Locate and identify every blood parasite.
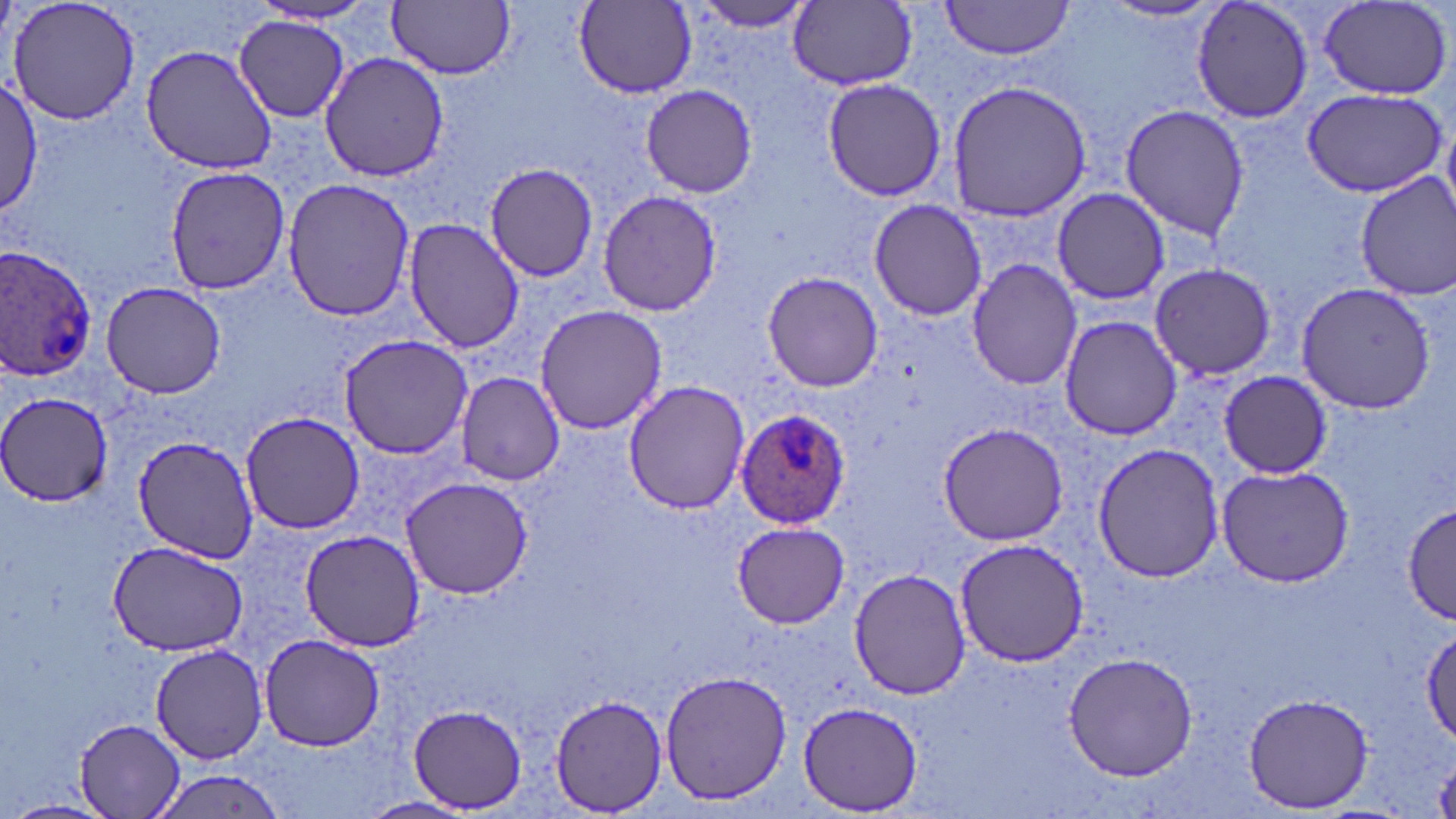
Approximate bounding boxes as (x1,y1)-(x2,y2) corner pairs in pixels.
Plasmodium ovale-infected red blood cells: (0,246)-(99,381), (736,411)-(850,527).
No Plasmodium falciparum, Plasmodium malariae, Plasmodium vivax, Babesia divergens, or Trypanosoma brucei observed.

slide_level_diagnosis: Plasmodium ovale
uninfected_red_blood_cell_locations: 'approximate bounding boxes as (x1,y1)-(x2,y2) corner pairs in pixels: (5,0)-(142,126), (686,0)-(817,34), (940,0)-(1074,60), (1190,0)-(1315,124), (388,1)-(516,79), (1101,1)-(1223,23), (575,2)-(697,97), (791,2)-(919,89), (1318,2)-(1453,100), (246,3)-(382,29), (235,17)-(350,123), (141,45)-(274,174), (320,52)-(448,182), (1,78)-(42,217), (820,79)-(948,202), (946,79)-(1095,221), (641,85)-(759,197), (1301,87)-(1448,199), (1119,103)-(1248,241), (485,163)-(600,280), (165,166)-(291,296), (1354,172)-(1456,301), (282,177)-(416,322), (1051,187)-(1170,306), (596,190)-(724,316), (867,199)-(988,320), (404,218)-(522,354), (967,260)-(1083,392), (1149,262)-(1278,381), (761,270)-(884,392), (101,280)-(227,399), (1296,282)-(1436,415), (534,304)-(667,434), (1058,315)-(1181,441), (340,334)-(474,459), (1217,370)-(1334,477), (456,373)-(564,486), (624,380)-(749,514), (2,394)-(114,508), (240,410)-(365,534), (938,422)-(1068,546), (134,437)-(260,564), (1091,442)-(1226,582), (1215,463)-(1356,587), (400,477)-(532,599), (1402,503)-(1453,625), (733,521)-(852,628), (300,531)-(426,650), (954,537)-(1092,667), (105,539)-(247,658), (848,567)-(971,700), (1423,628)-(1456,745), (261,635)-(384,750), (151,644)-(266,763), (1064,652)-(1198,781), (661,668)-(792,807), (1242,691)-(1374,813), (550,694)-(667,812), (800,702)-(923,814), (409,705)-(527,813), (74,717)-(188,819), (147,767)-(292,818), (357,796)-(478,819), (1,799)-(124,819)'
field_of_view: single
magnification: 1000x
image_size: 1456×819 pixels
preparation: thin blood smear
modality: light microscopy
stain: May-Grünwald-Giemsa